Find each parasitized red blood cell.
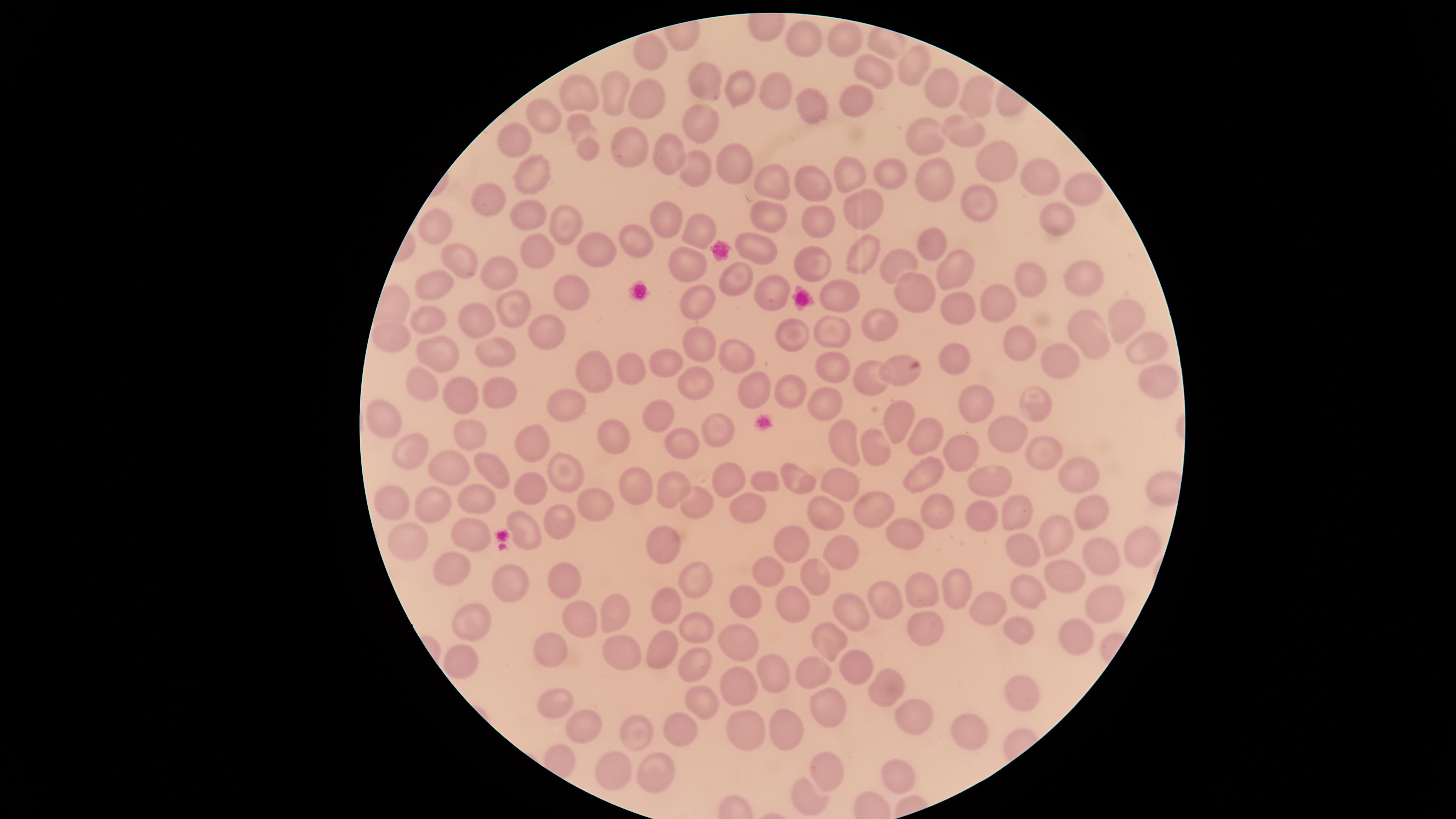
No parasitized red blood cells identified.

visible region = circular
stain = Giemsa
uninfected red blood cells = approximate marker points as (x, y) in pixels: (798, 35), (844, 37), (643, 56), (911, 63), (873, 69), (701, 81), (740, 82), (776, 87), (939, 88), (579, 95), (608, 96), (971, 96), (653, 101), (854, 102), (807, 104), (542, 113), (700, 125), (964, 131), (584, 137), (918, 137), (512, 143), (630, 143), (670, 154), (998, 161), (738, 163), (1036, 170), (534, 173), (693, 173), (852, 174), (891, 174), (926, 179), (810, 182), (1082, 189), (778, 190), (977, 198), (488, 200), (863, 207), (523, 214), (666, 215), (821, 219), (1054, 219), (771, 220), (566, 222), (439, 225), (693, 228), (933, 242), (641, 243), (754, 249), (593, 250), (863, 257), (539, 259), (686, 260), (895, 260), (456, 264), (958, 267), (813, 268), (1078, 270), (504, 271), (732, 278), (1030, 279), (432, 284), (770, 284), (573, 286), (909, 288), (833, 295), (692, 302), (993, 302), (512, 305), (958, 310), (1118, 315), (472, 317), (430, 319), (876, 321), (831, 331), (549, 332), (1091, 334), (393, 336), (787, 338), (695, 340), (1016, 343), (1143, 344), (492, 350), (442, 355), (734, 355), (951, 355), (1059, 357), (666, 359), (831, 365), (594, 367), (630, 368), (897, 368), (877, 376), (690, 377), (1157, 378), (422, 381), (462, 391), (755, 391), (793, 391), (498, 395), (974, 397), (563, 402), (822, 402), (1031, 403), (663, 412), (905, 418), (383, 421), (472, 429), (721, 429), (928, 429), (612, 430), (1008, 434), (533, 440), (877, 441), (846, 443), (687, 444), (416, 449), (962, 451), (1045, 453), (456, 469), (564, 469), (492, 470), (1085, 471), (919, 472), (799, 478), (770, 479), (990, 481), (640, 482), (672, 482), (731, 482), (837, 484), (530, 489), (480, 500), (874, 502), (393, 503), (588, 503), (694, 503), (429, 504), (1087, 505), (936, 506), (1017, 508), (747, 509), (826, 512), (985, 514), (556, 520), (526, 524), (1054, 524), (465, 529), (900, 532), (400, 537), (790, 541), (1020, 543), (1139, 543), (659, 546), (849, 546), (1102, 557), (456, 561), (1062, 569), (769, 570), (815, 573), (560, 577), (693, 577), (959, 582), (516, 584), (1027, 588), (919, 590), (883, 595), (672, 599), (1101, 600), (797, 601), (747, 604), (986, 605), (844, 606), (609, 607), (465, 617), (577, 617), (690, 624), (930, 625), (1020, 630), (1079, 638), (829, 641), (619, 643), (738, 643), (661, 646), (558, 651), (461, 660), (704, 664), (858, 664), (814, 669), (768, 671), (886, 689), (1016, 690), (748, 691), (556, 698), (821, 701), (697, 705), (915, 713), (581, 726), (794, 728), (682, 729), (747, 729), (967, 731), (638, 735), (613, 768), (831, 769), (894, 773), (657, 775), (806, 797)
image size = 1456×819 pixels
preparation = thin blood smear
capture = smartphone photograph through the microscope eyepiece
field of view = single